Outline each blood parasite and name the species.
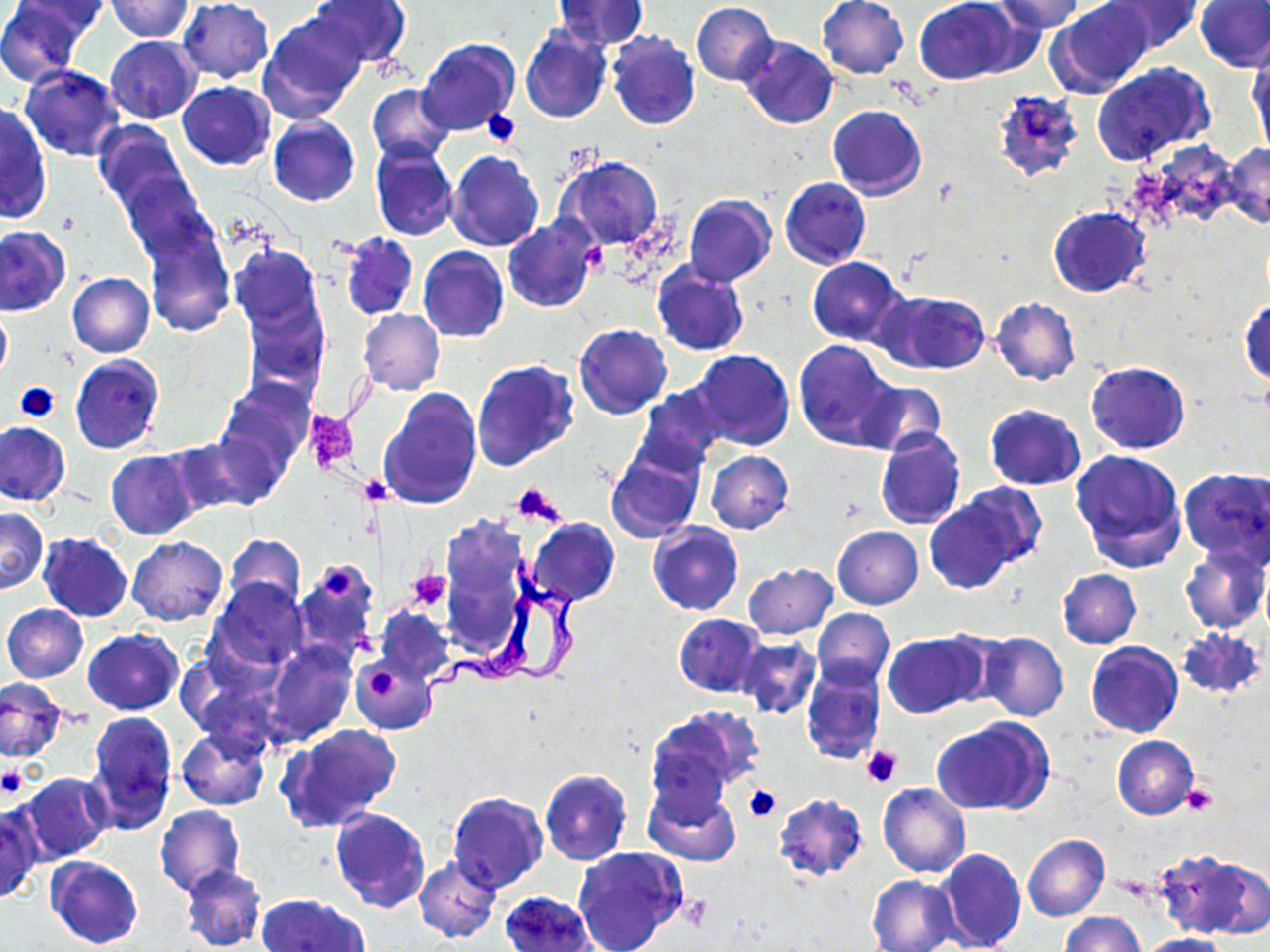

Approximate bounding boxes as [x1, y1, x2, y2] in pixels.
Trypanosoma brucei: [438, 519, 534, 663], [406, 546, 598, 726].
No Plasmodium falciparum, Plasmodium ovale, Plasmodium malariae, Plasmodium vivax, or Babesia divergens observed.

Platelet locations: [481, 109, 520, 147], [579, 243, 609, 273], [15, 382, 59, 423], [305, 408, 359, 473], [357, 474, 392, 505], [512, 482, 564, 527], [323, 568, 355, 600], [407, 569, 452, 612], [370, 667, 398, 700], [859, 745, 903, 787], [0, 767, 27, 798], [1182, 784, 1218, 816], [743, 785, 780, 823]. Uninfected red blood cell locations: [0, 0, 90, 86], [15, 0, 111, 36], [105, 0, 195, 41], [178, 0, 274, 82], [307, 0, 411, 68], [551, 0, 649, 51], [817, 0, 909, 79], [915, 0, 1020, 84], [991, 0, 1087, 33], [1047, 0, 1156, 98], [1103, 0, 1201, 53], [1195, 1, 1270, 72], [690, 2, 779, 86], [259, 12, 366, 124], [521, 26, 612, 123], [606, 31, 700, 130], [105, 35, 202, 123], [417, 37, 519, 138], [738, 37, 838, 131], [1247, 49, 1269, 155], [1092, 62, 1213, 164], [20, 65, 123, 161], [177, 81, 276, 168], [367, 84, 454, 163], [1, 103, 51, 224], [827, 105, 927, 200], [268, 117, 360, 207], [92, 120, 191, 216], [1139, 140, 1240, 231], [370, 143, 459, 241], [1224, 144, 1270, 228], [447, 150, 544, 251], [555, 155, 665, 250], [115, 170, 218, 268], [780, 177, 871, 269], [684, 194, 777, 286], [1047, 207, 1150, 298], [503, 213, 599, 312], [143, 225, 235, 337], [0, 227, 70, 315], [339, 231, 417, 320], [230, 244, 326, 336], [417, 246, 509, 342], [807, 256, 906, 345], [652, 260, 749, 356], [67, 272, 155, 358], [879, 289, 990, 375], [241, 295, 329, 402], [991, 298, 1080, 385], [1240, 299, 1269, 388], [0, 305, 11, 383], [359, 310, 444, 396], [574, 323, 673, 420], [793, 339, 898, 451], [688, 349, 797, 452], [69, 354, 165, 453], [471, 358, 580, 470], [1086, 362, 1189, 454], [218, 379, 313, 471], [857, 381, 945, 457], [636, 385, 728, 472], [379, 387, 481, 511], [984, 403, 1086, 490], [1, 422, 70, 506], [193, 430, 291, 511], [874, 430, 965, 530], [163, 436, 254, 518], [604, 443, 705, 542], [1070, 448, 1187, 571], [107, 450, 200, 539], [706, 450, 794, 534], [1180, 468, 1269, 565], [953, 483, 1044, 572], [923, 495, 1026, 593], [0, 508, 47, 592], [527, 518, 620, 607], [648, 522, 743, 615], [832, 525, 924, 610], [38, 532, 132, 622], [225, 534, 306, 614], [127, 537, 228, 626], [1179, 545, 1269, 635], [291, 559, 380, 661], [742, 563, 837, 639], [1058, 569, 1140, 647], [210, 579, 308, 671], [2, 604, 88, 682], [376, 608, 453, 683], [811, 609, 894, 687], [673, 613, 764, 696], [1175, 627, 1265, 700], [83, 629, 183, 715], [883, 632, 986, 719], [978, 632, 1067, 721], [735, 637, 820, 719], [1085, 640, 1183, 738], [265, 642, 355, 744], [350, 657, 435, 735], [801, 665, 885, 764], [0, 678, 66, 762], [646, 707, 757, 811], [84, 713, 177, 832], [933, 717, 1052, 816], [278, 723, 402, 831], [177, 728, 270, 810], [1112, 735, 1198, 818], [550, 766, 651, 933], [539, 770, 633, 866], [18, 772, 111, 864], [644, 782, 740, 866], [878, 783, 970, 878], [447, 792, 548, 895], [773, 793, 868, 882], [0, 800, 41, 904], [154, 805, 244, 898], [329, 808, 430, 913], [1022, 834, 1110, 921], [571, 846, 687, 952], [934, 848, 1025, 951], [1155, 848, 1268, 939], [45, 856, 142, 948], [415, 856, 500, 941], [180, 865, 265, 951], [866, 874, 959, 952], [500, 890, 597, 952], [256, 893, 368, 952], [1061, 912, 1146, 952], [1134, 931, 1233, 952]. Slide-level diagnosis: Trypanosoma brucei. May-Grünwald-Giemsa-stained preparation. Thin blood film. Optical microscopy. Captured at 1000x magnification. Image is 1270×952 pixels. One field of a larger specimen.